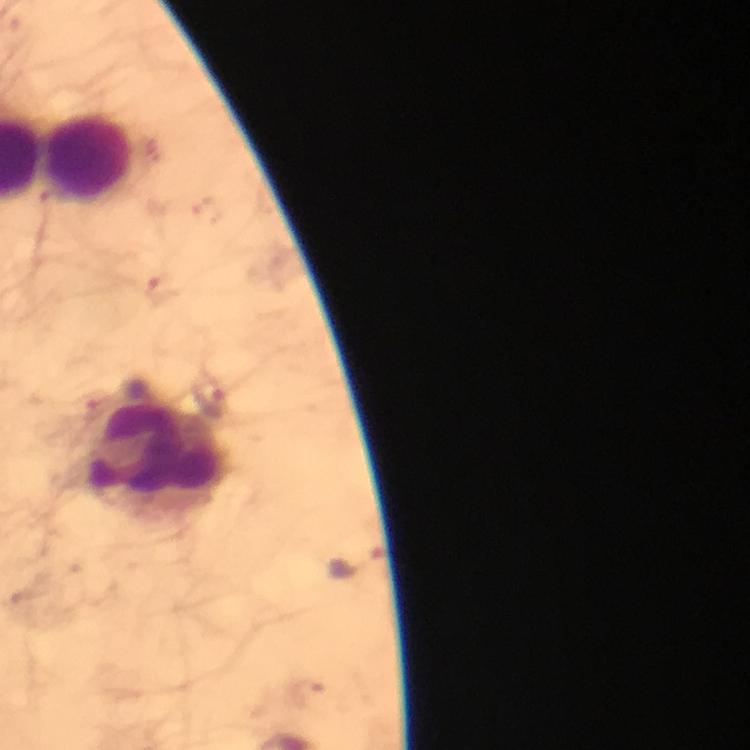

Approximate centers as {x, y} in pixels.
Summary:
  - Leukocyte locations: {91, 153}, {154, 458}
  - Plasmodium parasite locations: {165, 290}, {358, 563}, {307, 692}
  - Immersion oil: applied
  - Context: from a malaria diagnostic workup
  - Image size: 750×750 pixels
  - Preparation: thick blood film
  - Stain: Giemsa
  - Cropped from: a single field of view
  - Magnification: 100x
  - Capture: smartphone camera through the microscope